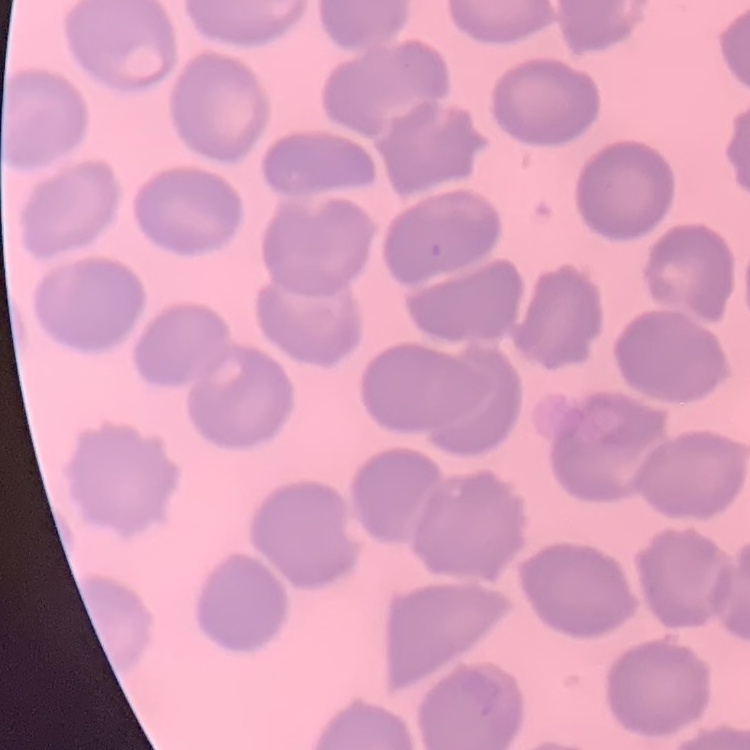

Summary:
  - Erythrocyte morphology: no rouleaux formation
  - Preparation: thin blood smear
  - Image type: one tile cut from a larger photomicrograph
  - Stain: Field's or Giemsa